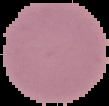 Image is 109×106 pixels. Malaria status: uninfected. From a thin blood smear. Segmented cell region on a black background.